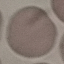
Malaria status: uninfected. Thin smear of blood. Photographed with a smartphone camera at the microscope eyepiece. Giemsa stain. Automatically extracted cell patch, resized to 64 × 64 pixels.